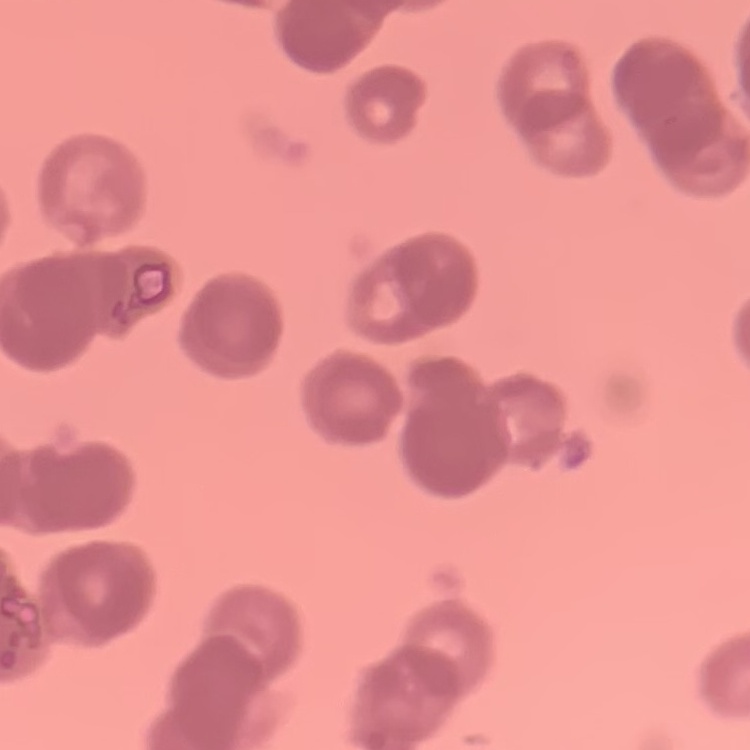
Summary:
  - Erythrocyte morphology: rouleaux formation
  - Stain: Field's or Giemsa
  - Preparation: thin blood smear
  - Image type: square crop of a larger photomicrograph